Give the position of every Plasmodium parasite.
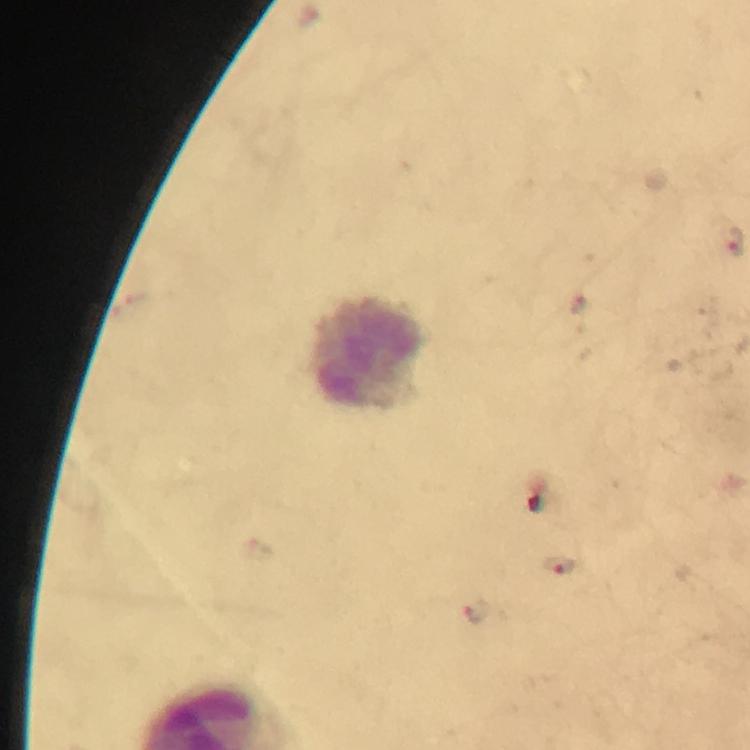

Approximate object centers, in pixels from the top-left corner.
Plasmodium parasites: (x=560, y=564), (x=476, y=612).

Leukocyte locations: (x=368, y=355). Cropped region of a single field of view. Thick smear. Immersion oil applied. From a malaria diagnostic workup. Image is 750×750 pixels. Photographed through the microscope with a smartphone camera. Giemsa stain. 100x magnification.